Outline each Plasmodium falciparum parasite and classify it by life-cycle stage.
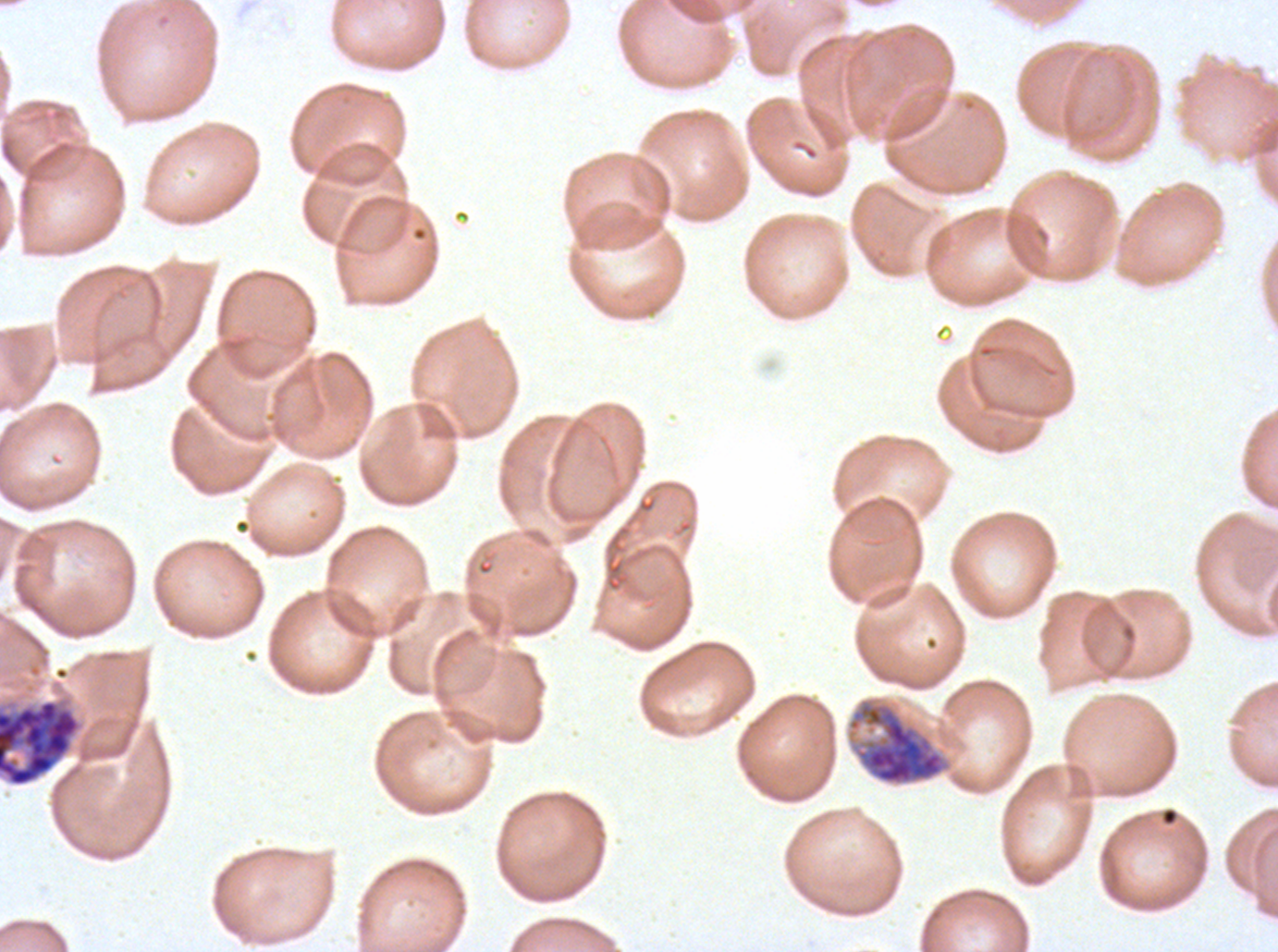
Approximate bounding boxes as {x1, y1, x2, y2} in pixels.
Early schizonts: {846, 696, 952, 787}.
Segmenters: {0, 698, 82, 787}.
No rings, late-ring/early-trophozoite forms, mid trophozoites, late trophozoites, late schizonts, or gametocytes observed.

Summary:
  - Specimen: ex-vivo Plasmodium falciparum culture from a patient in The Gambia, grown for 24 to 48 hours
  - Stain: Giemsa
  - Life-cycle stages observed: early schizont, segmenter
  - Preparation: thin blood film
  - Image size: 1278×952 pixels
  - Field of view: sub-image separated from a larger composite